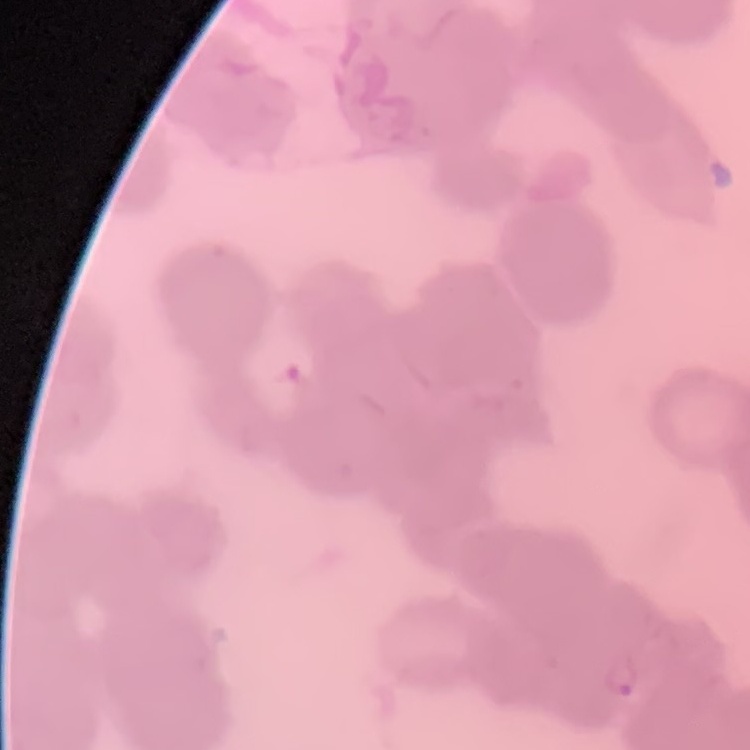

The red blood cells exhibit rouleaux formation. Square crop of a larger photomicrograph. Thin blood smear. Stained with either Field's or Giemsa.